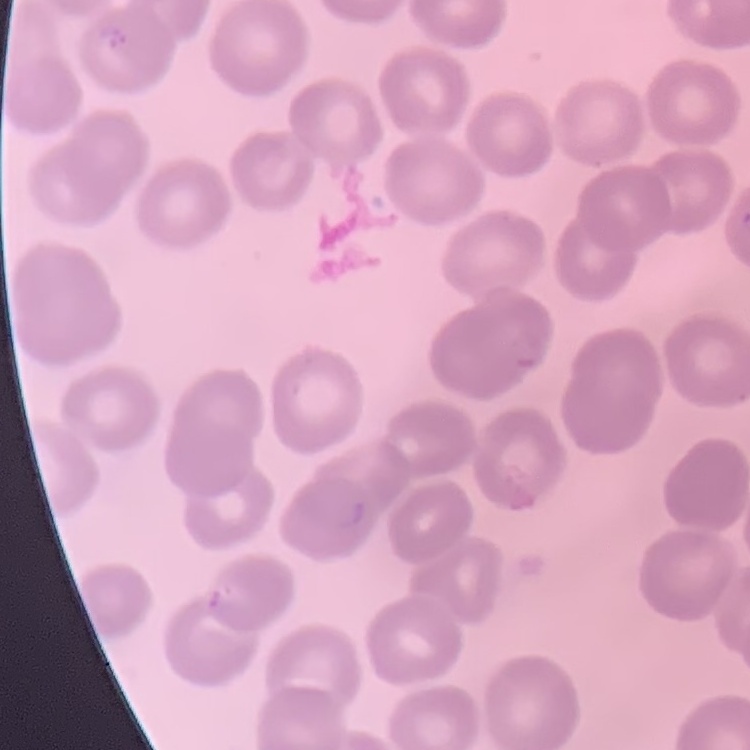

Summary:
  - Red blood cell morphology: no rouleaux formation
  - Stain: Field's or Giemsa
  - Preparation: thin peripheral smear
  - Image type: one tile cut from a larger photomicrograph